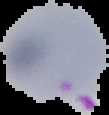
Summary:
  - Image type: segmented cell region with the area outside set to black
  - Preparation: thin blood smear
  - Image size: 109×115 pixels
  - Malaria status: parasitized